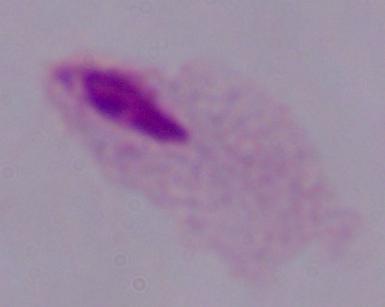 A trichomonad is shown. Photomicrograph. 1000x magnification.